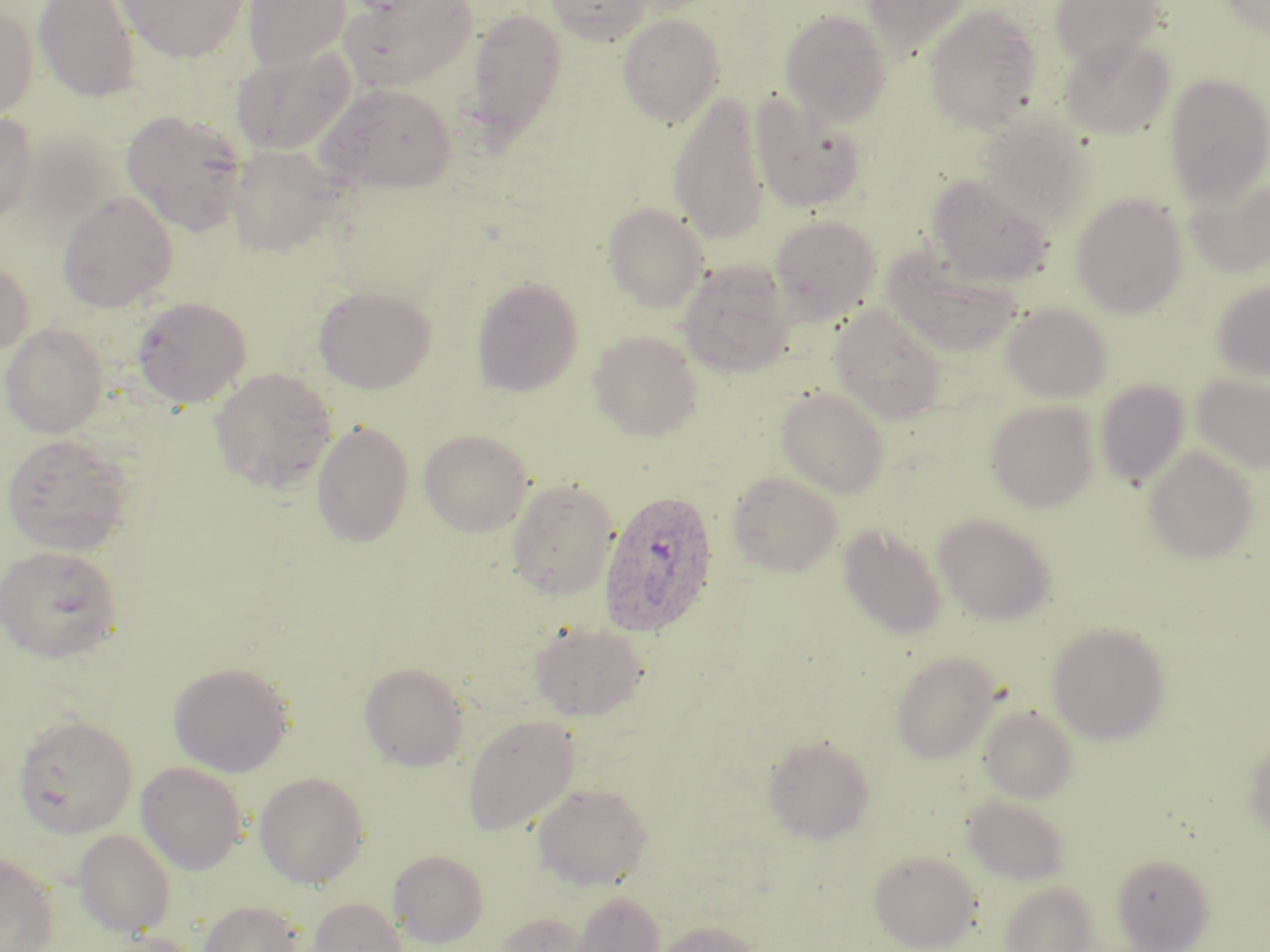

Summary:
  - Coordinate format: approximate bounding boxes as (x1, y1, x2, y2) in pixels
  - Uninfected red blood cell locations: (34, 0, 141, 102), (115, 0, 251, 62), (242, 0, 351, 69), (546, 0, 651, 45), (859, 0, 975, 58), (1048, 0, 1165, 69), (1218, 0, 1270, 36), (342, 1, 479, 92), (0, 4, 39, 120), (923, 4, 1043, 134), (464, 7, 568, 143), (780, 9, 891, 125), (617, 13, 725, 127), (1060, 36, 1175, 139), (231, 45, 356, 156), (1164, 73, 1269, 205), (316, 83, 455, 192), (668, 91, 771, 244), (749, 93, 867, 214), (121, 109, 250, 236), (0, 112, 37, 225), (976, 112, 1097, 229), (226, 143, 344, 256), (926, 174, 1053, 287), (1186, 175, 1270, 278), (57, 190, 178, 312), (1070, 193, 1188, 317), (604, 202, 709, 313), (770, 214, 880, 322), (882, 252, 1021, 356), (0, 258, 34, 359), (678, 260, 796, 377), (470, 275, 584, 397), (1211, 281, 1270, 381), (313, 285, 436, 393), (132, 296, 252, 408), (1002, 302, 1112, 401), (831, 306, 947, 422), (0, 322, 108, 438), (588, 331, 703, 441), (210, 367, 337, 493), (1191, 372, 1270, 472), (1095, 380, 1190, 486), (776, 386, 890, 497), (985, 399, 1099, 513), (311, 421, 414, 547), (418, 428, 534, 537), (1, 433, 137, 556), (1143, 446, 1259, 563), (727, 472, 842, 576), (507, 478, 619, 599), (933, 513, 1056, 624), (839, 525, 947, 639), (1, 545, 123, 662), (529, 621, 649, 721), (1046, 621, 1170, 743), (890, 650, 1001, 763), (168, 662, 294, 777), (359, 662, 468, 771), (978, 704, 1079, 803), (12, 713, 139, 838), (463, 715, 580, 835), (763, 734, 875, 844), (1243, 738, 1270, 842), (135, 762, 247, 874), (254, 772, 370, 889), (532, 782, 655, 890), (962, 795, 1070, 885), (73, 830, 177, 937), (388, 849, 489, 948), (868, 849, 981, 951), (0, 853, 60, 952), (1112, 853, 1214, 951), (998, 880, 1100, 952), (570, 890, 665, 952), (306, 897, 408, 952), (198, 899, 308, 952), (493, 911, 593, 952), (653, 919, 761, 952), (91, 931, 205, 952)
  - Plasmodium ovale-infected red blood cell locations: (598, 488, 721, 637)
  - Slide-level diagnosis: Plasmodium ovale
  - Field of view: one of a larger specimen
  - Stain: May-Grünwald-Giemsa
  - Image size: 1270×952 pixels
  - Magnification: 1000x
  - Preparation: thin blood smear
  - Modality: light microscopy